Name the parasite shown.
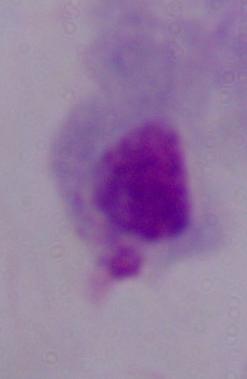
This is a trichomonad.

Summary:
  - Modality: micrograph
  - Magnification: 1000x